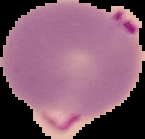
{
  "preparation": "thin blood film",
  "result": "Plasmodium parasites identified",
  "image_size": "145×139 pixels",
  "image_type": "segmented cell region with the area outside set to black"
}